Describe the morphology of the red blood cells.
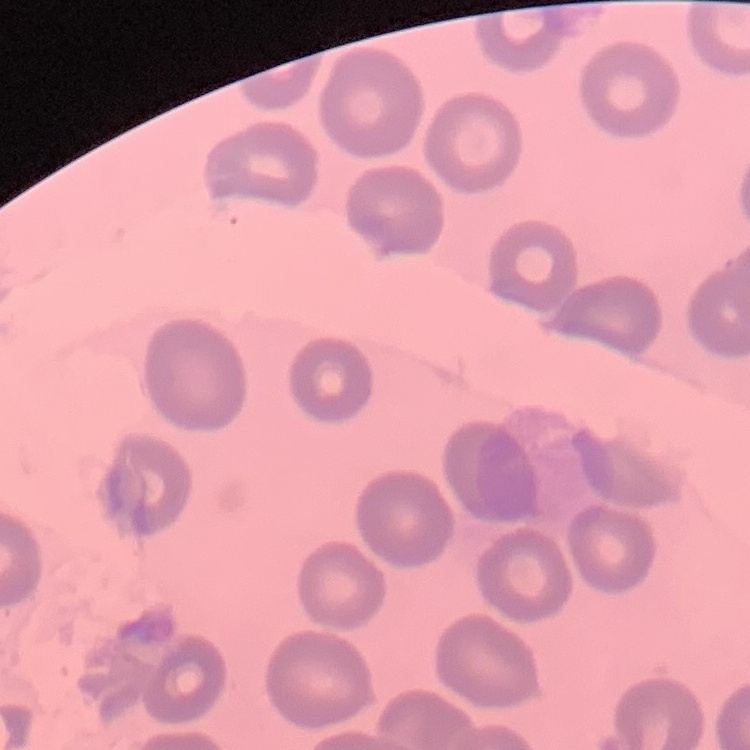

They show no rouleaux formation.

Thin blood smear. Stained with either Field's or Giemsa. Square crop of a larger photomicrograph.